Locate every blood parasite and identify its species.
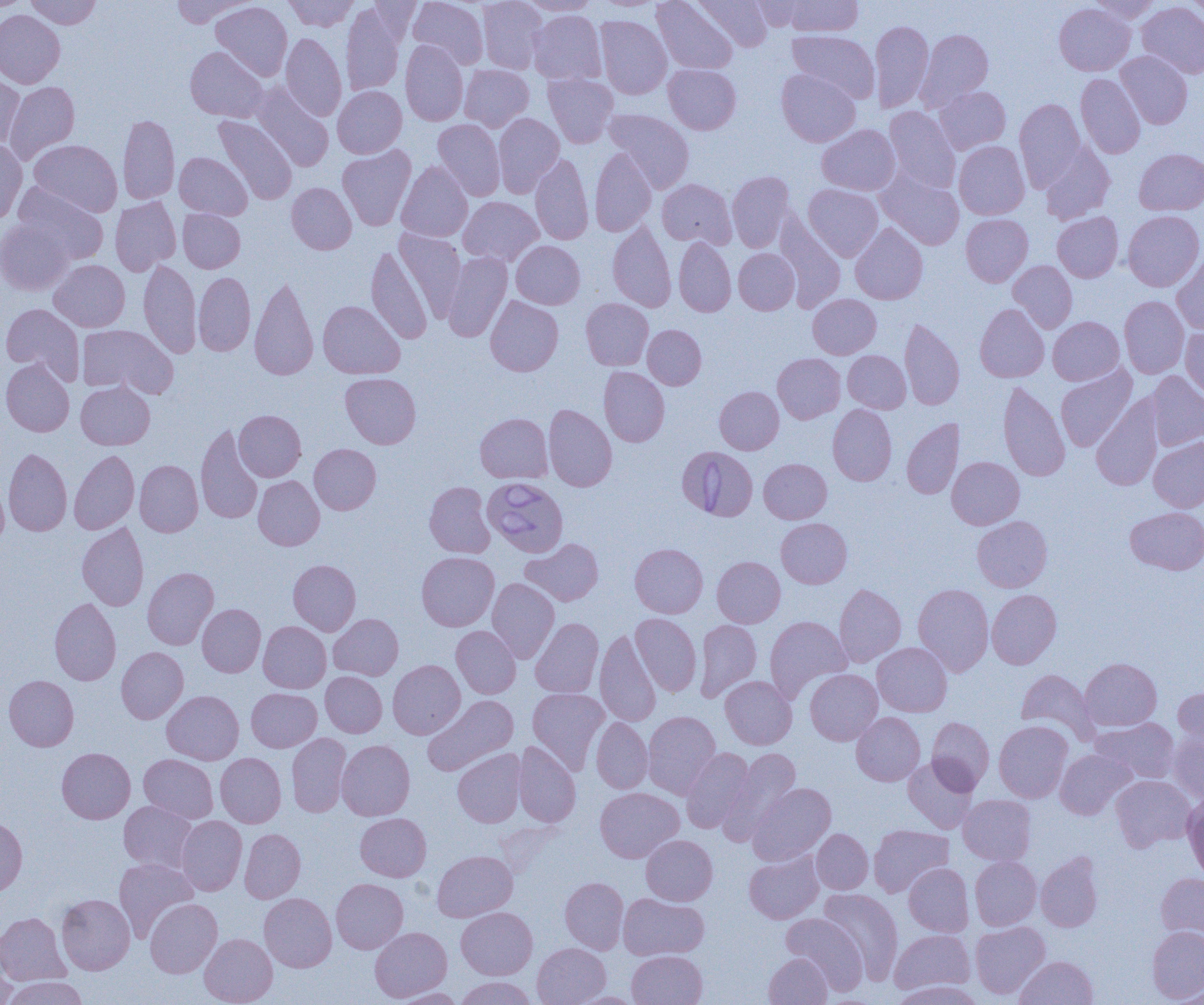

Approximate bounding boxes as (x1,y1)-(x2,y2) corner pairs in pixels.
Babesia divergens-infected red blood cells: (678,446)-(758,520), (483,477)-(568,557).
No Plasmodium falciparum, Plasmodium ovale, Plasmodium malariae, Plasmodium vivax, or Trypanosoma brucei observed.

Uninfected red blood cell locations: (25,0)-(101,29), (170,0)-(251,27), (284,0)-(359,31), (408,0)-(488,69), (477,0)-(547,74), (518,0)-(602,16), (652,0)-(738,74), (693,0)-(773,52), (750,0)-(811,31), (783,0)-(863,37), (1088,0)-(1162,24), (1186,0)-(1204,25), (0,1)-(25,13), (211,1)-(292,81), (1054,2)-(1135,75), (1137,2)-(1204,78), (341,4)-(407,96), (0,10)-(65,88), (528,10)-(606,85), (595,15)-(671,99), (870,19)-(934,112), (916,29)-(993,110), (787,30)-(880,103), (281,33)-(347,121), (400,40)-(468,126), (185,46)-(268,122), (1115,51)-(1192,128), (663,63)-(741,134), (460,64)-(534,131), (777,69)-(860,147), (0,73)-(25,151), (1076,73)-(1145,158), (543,74)-(618,147), (3,81)-(80,165), (252,83)-(333,172), (333,86)-(407,158), (934,86)-(1010,154), (1014,98)-(1085,190), (884,106)-(961,193), (604,109)-(695,193), (493,113)-(564,197), (118,114)-(180,204), (213,115)-(297,204), (433,119)-(505,200), (817,124)-(900,195), (0,139)-(27,226), (29,140)-(122,217), (954,141)-(1029,219), (1040,142)-(1115,224), (337,146)-(416,230), (590,148)-(657,237), (1134,149)-(1204,215), (174,152)-(252,220), (530,153)-(593,245), (396,161)-(473,242), (727,171)-(795,252), (876,171)-(964,250), (658,179)-(736,248), (12,183)-(108,265), (286,183)-(357,254), (803,184)-(883,261), (110,196)-(181,275), (459,196)-(543,266), (178,209)-(245,272), (1123,210)-(1204,292), (1052,211)-(1123,282), (775,213)-(845,311), (960,213)-(1033,286), (0,220)-(74,294), (608,222)-(676,312), (850,223)-(928,304), (395,229)-(467,320), (674,238)-(736,316), (511,241)-(585,309), (365,246)-(433,344), (734,249)-(799,314), (1171,250)-(1204,335), (442,252)-(512,342), (138,259)-(201,357), (49,260)-(130,332), (1008,260)-(1077,333), (194,272)-(255,356), (249,274)-(319,380), (808,294)-(881,359), (485,296)-(563,376), (1119,296)-(1189,378), (581,298)-(654,370), (318,300)-(404,379), (1,303)-(84,384), (975,303)-(1049,382), (1048,317)-(1124,385), (899,318)-(965,410), (77,324)-(177,398), (643,325)-(706,389), (1180,325)-(1204,403), (843,350)-(911,413), (772,353)-(845,423), (1,358)-(74,437), (1056,364)-(1137,452), (599,366)-(669,447), (1145,371)-(1204,451), (340,372)-(421,448), (76,381)-(155,450), (998,382)-(1070,481), (715,386)-(784,454), (1091,396)-(1164,491), (543,404)-(616,492), (828,405)-(897,485), (234,410)-(306,481), (476,413)-(552,483), (902,418)-(964,499), (195,424)-(264,525), (1148,436)-(1204,512), (309,444)-(381,514), (3,448)-(72,536), (69,449)-(139,534), (947,456)-(1024,529), (759,458)-(831,523), (135,460)-(203,537), (0,473)-(9,552), (253,475)-(324,550), (424,481)-(495,558), (1125,507)-(1204,574), (972,515)-(1052,592), (776,518)-(852,588), (77,522)-(148,610), (521,538)-(603,606), (630,543)-(708,617), (417,552)-(499,631), (709,556)-(777,701), (712,556)-(785,627), (288,560)-(361,636), (142,567)-(218,649), (487,577)-(559,663), (913,583)-(993,676), (834,584)-(906,667), (987,589)-(1061,669), (50,598)-(121,685), (197,603)-(265,677), (329,613)-(404,680), (631,614)-(701,696), (765,616)-(852,702), (530,618)-(604,698), (694,619)-(762,702), (258,621)-(331,693), (451,626)-(521,698), (594,630)-(661,726), (872,642)-(952,717), (116,647)-(188,723), (1080,658)-(1161,730), (388,660)-(465,738), (805,668)-(882,745), (1016,669)-(1098,743), (320,672)-(387,737), (4,675)-(79,751), (720,675)-(797,749), (528,687)-(609,773), (1174,687)-(1204,748), (246,688)-(321,752), (162,690)-(244,764), (422,695)-(518,776), (643,711)-(720,798), (851,712)-(925,786), (591,717)-(652,794), (926,717)-(994,793), (1092,718)-(1179,783), (994,720)-(1073,802), (287,732)-(351,817), (1169,733)-(1204,805), (337,739)-(414,820), (512,741)-(581,827), (57,747)-(135,823), (681,748)-(754,832), (718,748)-(801,845), (453,749)-(526,827), (1055,749)-(1136,820), (215,753)-(286,827), (139,754)-(218,823), (903,757)-(979,833), (1110,774)-(1196,851), (748,782)-(836,864), (595,787)-(684,863), (1183,793)-(1204,880), (958,795)-(1036,865), (119,801)-(198,873), (355,813)-(431,881), (0,816)-(27,896), (176,816)-(247,896), (868,825)-(953,897), (239,829)-(305,903), (811,829)-(873,894), (641,835)-(717,905), (744,849)-(824,923), (432,850)-(517,922), (1036,851)-(1103,932), (970,856)-(1041,930), (114,858)-(197,941), (904,863)-(973,936), (1156,873)-(1204,943), (560,877)-(628,954), (331,878)-(408,953), (819,888)-(903,982), (56,893)-(135,974), (259,893)-(337,972), (618,893)-(709,960), (145,898)-(222,977), (456,907)-(537,979), (781,912)-(868,993), (0,913)-(70,985), (970,921)-(1050,998), (370,926)-(451,1001), (1147,926)-(1204,1002), (889,929)-(975,994), (200,934)-(277,1005), (532,942)-(610,1005), (0,949)-(17,1005), (627,950)-(707,1005), (764,953)-(833,1004), (1016,956)-(1098,1005), (3,977)-(88,1005), (455,977)-(537,1005), (891,980)-(983,1005), (1168,986)-(1204,1005), (392,987)-(467,1004). Slide-level diagnosis: Babesia divergens. Optical microscopy. Thin blood film. Image is 1204×1005 pixels. 1000x magnification. Single field of view.